Identify the parasite.
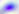
Toxoplasma gondii.

modality = micrograph
magnification = 400x